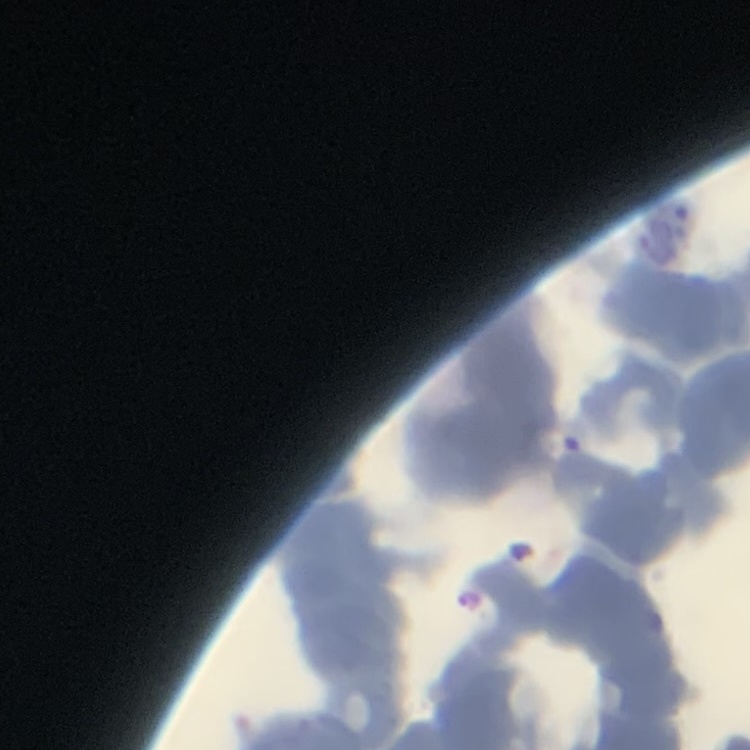

erythrocyte_morphology: rouleaux formation
image_type: one tile cut from a larger photomicrograph
stain: Field's or Giemsa
preparation: thin peripheral smear